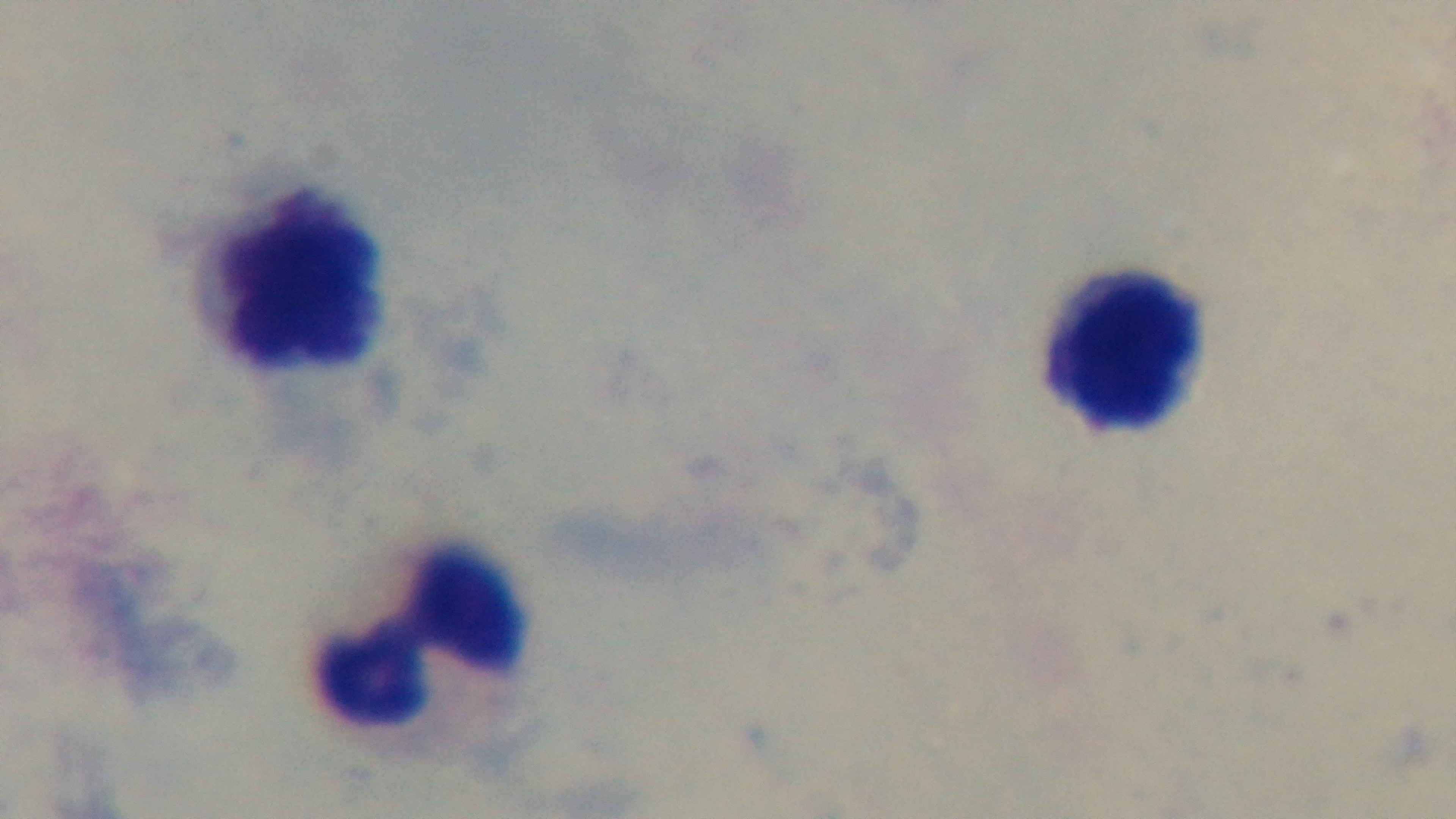
objective = 100x oil immersion
field of view = single
malaria status = negative
preparation = thick blood film
modality = light microscopy
capture = mounted 4K digital camera
stain = Giemsa